Locate every leukocyte (white blood cell).
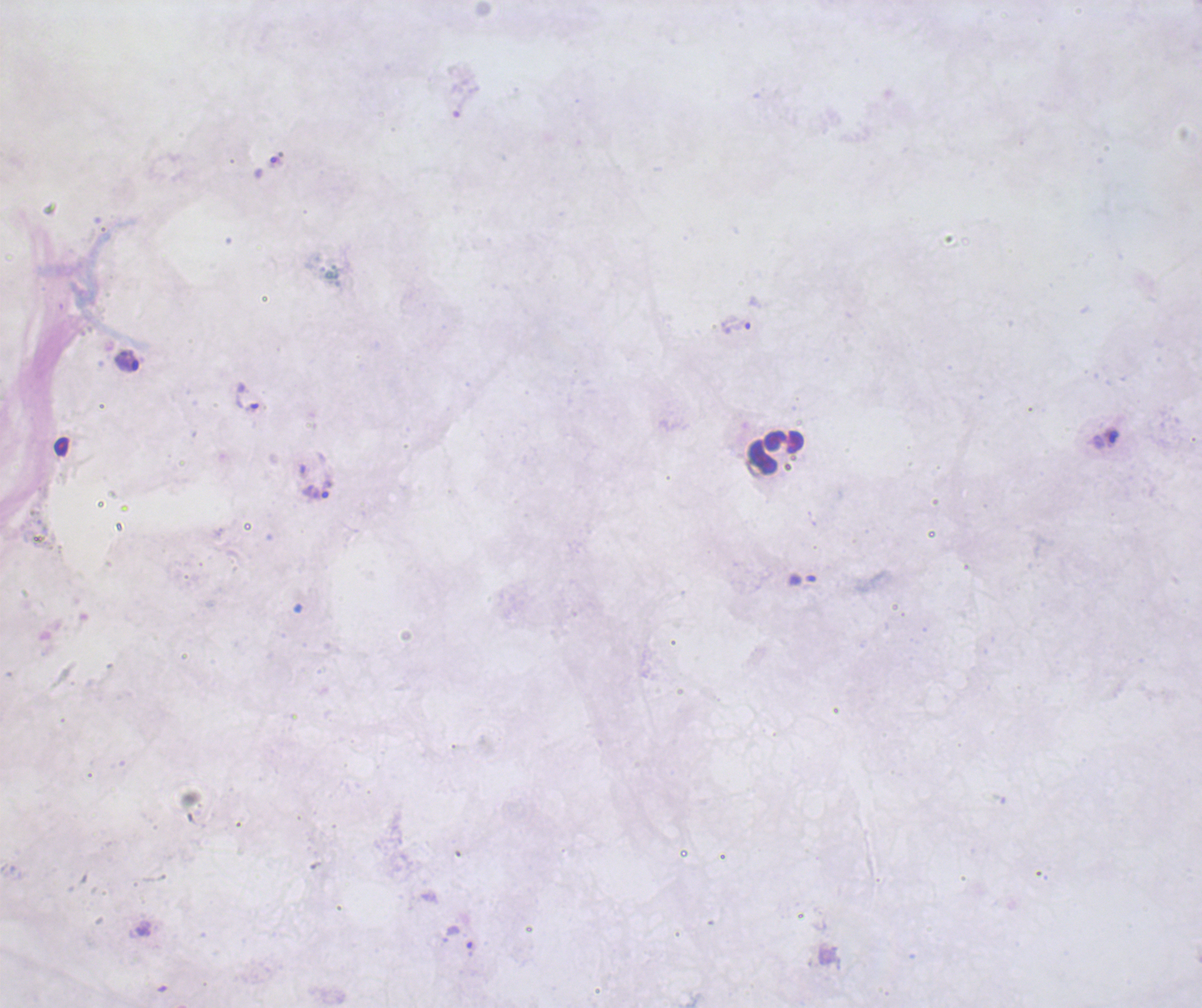
Approximate centers as [x, y] in pixels.
Leukocytes: [776, 452].

Approximate centers as [x, y] in pixels. Trophozoite locations: [736, 324], [128, 361], [247, 396], [315, 491]. Thick blood film. Single field of view. Background quality: unsatisfactory. Previously used in a real diagnosis. Coloration quality: bad. Result: Plasmodium parasites detected. 100x magnification. Romanowsky stain. Image is 1202×1008 pixels.